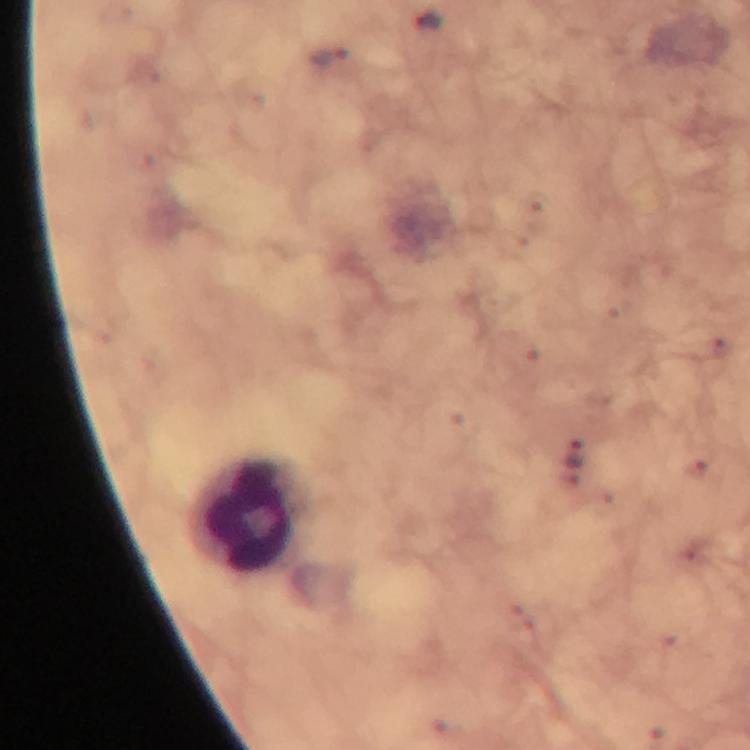

stain = Giemsa
leukocyte locations = approximate centers as (x, y) in pixels: (245, 515)
context = from a malaria diagnostic workup
immersion oil = used
magnification = 100x
image size = 750×750 pixels
capture = smartphone camera through the microscope
preparation = thick blood film
cropped from = a single field of view
malaria parasite locations = approximate centers as (x, y) in pixels: (330, 57), (575, 453)